Outline each blood parasite and name the species.
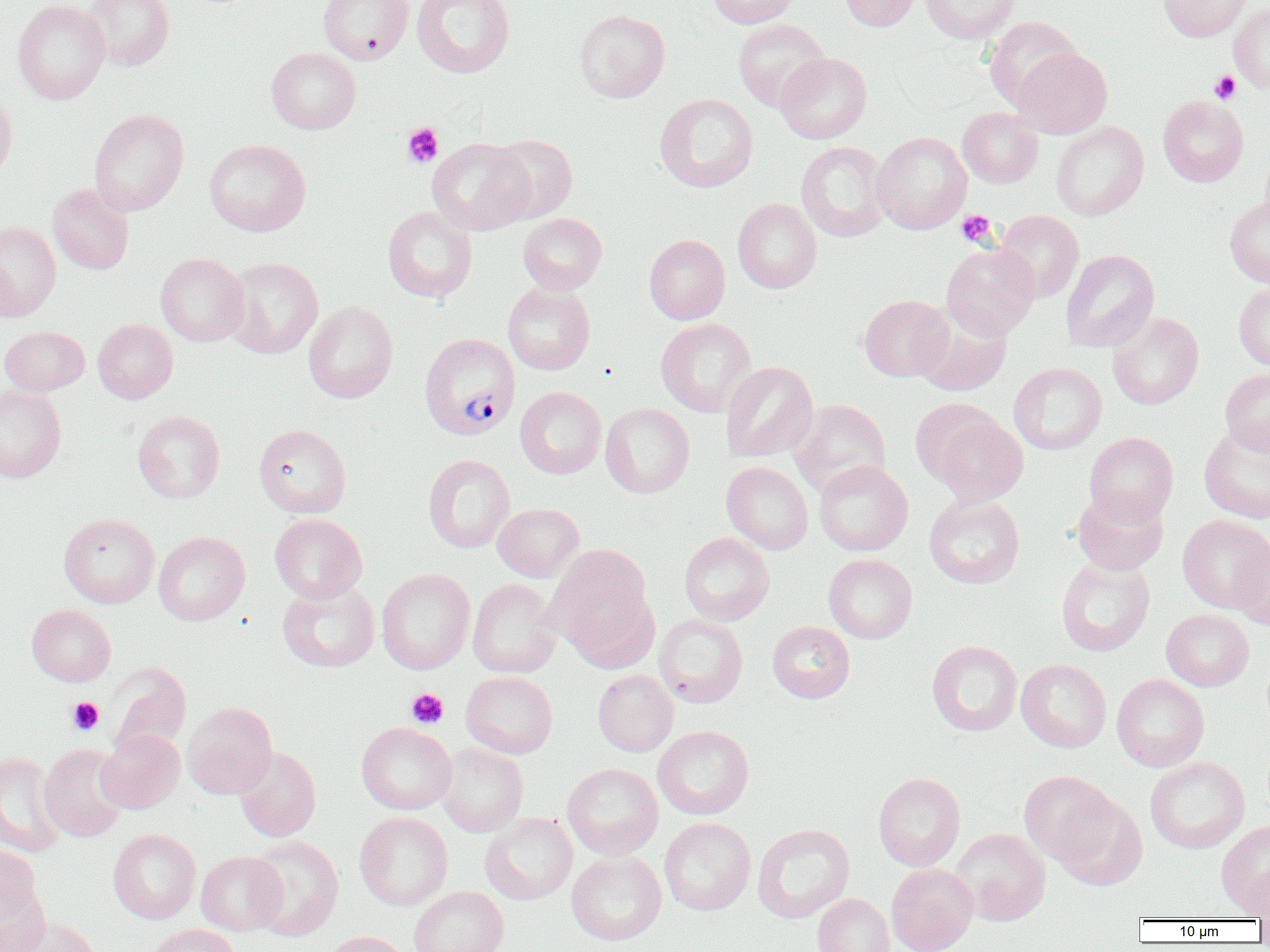
Approximate bounding boxes as (x1,y1)-(x2,y2) corner pairs in pixels.
Plasmodium vivax-infected red blood cells: (419,333)-(520,440).
No Plasmodium falciparum, Plasmodium ovale, Plasmodium malariae, Babesia divergens, or Trypanosoma brucei observed.

Summary:
  - Platelet locations: (1209,70)-(1241,105), (402,122)-(444,168), (956,210)-(997,247), (407,687)-(449,729), (66,696)-(104,736)
  - Uninfected red blood cell locations: (12,0)-(109,105), (82,0)-(174,71), (318,0)-(413,64), (412,0)-(515,78), (707,0)-(797,28), (839,0)-(920,32), (920,0)-(1022,44), (1158,0)-(1251,42), (1229,3)-(1270,93), (574,9)-(670,103), (983,16)-(1082,111), (733,19)-(830,112), (266,47)-(361,134), (1011,47)-(1112,138), (774,52)-(871,144), (0,88)-(17,181), (655,93)-(757,192), (1158,96)-(1248,187), (957,107)-(1043,188), (89,109)-(188,217), (1051,121)-(1149,220), (871,132)-(972,234), (487,134)-(578,223), (426,138)-(533,235), (204,139)-(311,236), (795,141)-(892,242), (1259,142)-(1270,233), (47,184)-(134,275), (1224,196)-(1270,288), (733,198)-(822,294), (382,206)-(477,303), (995,210)-(1084,302), (518,213)-(607,295), (0,221)-(61,320), (644,234)-(730,324), (941,242)-(1040,340), (1061,249)-(1159,352), (156,253)-(249,346), (222,257)-(323,358), (503,282)-(595,375), (1234,282)-(1270,372), (859,294)-(953,382), (303,300)-(398,404), (916,312)-(1011,396), (1107,312)-(1204,410), (656,318)-(757,417), (92,319)-(178,403), (0,326)-(89,396), (720,361)-(818,463), (1009,362)-(1107,455), (1220,368)-(1270,456), (0,384)-(66,482), (515,386)-(606,478), (789,399)-(891,497), (600,403)-(694,498), (917,403)-(1027,504), (132,410)-(225,503), (1199,423)-(1270,523), (254,424)-(351,518), (1084,432)-(1179,525), (423,454)-(515,553), (814,460)-(913,556), (721,461)-(813,555), (1071,488)-(1169,575), (924,494)-(1025,589), (493,503)-(584,582), (59,513)-(159,608), (269,513)-(367,603), (1177,514)-(1270,612), (154,531)-(250,625), (679,532)-(774,626), (1232,537)-(1270,631), (551,553)-(658,672), (823,553)-(917,644), (1055,555)-(1155,656), (376,569)-(475,674), (467,578)-(562,678), (277,580)-(380,673), (26,604)-(116,686), (1161,609)-(1254,691), (654,614)-(748,707), (767,621)-(855,703), (926,640)-(1022,736), (1016,659)-(1111,752), (106,663)-(191,757), (592,669)-(678,757), (461,671)-(558,758), (1111,674)-(1209,771), (182,702)-(278,799), (356,722)-(456,814), (653,725)-(754,819), (96,729)-(185,813), (435,742)-(528,837), (39,744)-(130,842), (233,746)-(321,841), (0,752)-(66,856), (1145,756)-(1249,854), (562,763)-(663,860), (1019,770)-(1120,867), (873,772)-(965,871), (1053,791)-(1147,890), (355,811)-(453,910), (480,812)-(578,905), (659,817)-(756,915), (1216,819)-(1270,915), (752,823)-(855,923), (108,828)-(201,924), (951,828)-(1051,926), (245,835)-(344,940), (0,844)-(42,926), (566,850)-(666,945), (195,851)-(286,935), (1247,862)-(1270,924), (886,863)-(978,952), (0,884)-(52,952), (408,886)-(509,952), (812,893)-(894,952), (11,917)-(103,952), (147,924)-(241,952), (322,931)-(413,952)
  - Slide-level diagnosis: Plasmodium vivax
  - Modality: light microscopy
  - Preparation: thin blood smear
  - Magnification: 1000x
  - Field of view: single
  - Image size: 1270×952 pixels